State which parasite is depicted.
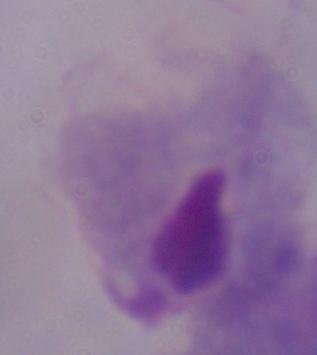
A trichomonad.

Captured at 1000x magnification. Photomicrograph.